Assess this cell for malaria.
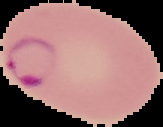
It is parasitized.

Summary:
  - Image size: 163×127 pixels
  - Preparation: thin blood smear
  - Image type: cell region segmented out of the field of view; surrounding area masked to black